Classify this cell by malaria status.
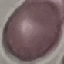
It is uninfected.

stain = Giemsa
capture = smartphone camera at the microscope eyepiece
preparation = thin smear
image type = automatically extracted cell patch, resized to 64 × 64 pixels